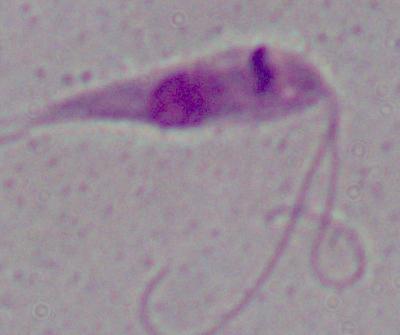
magnification: 1000x
identification: Leishmania
modality: photomicrograph